Name the blood parasite species.
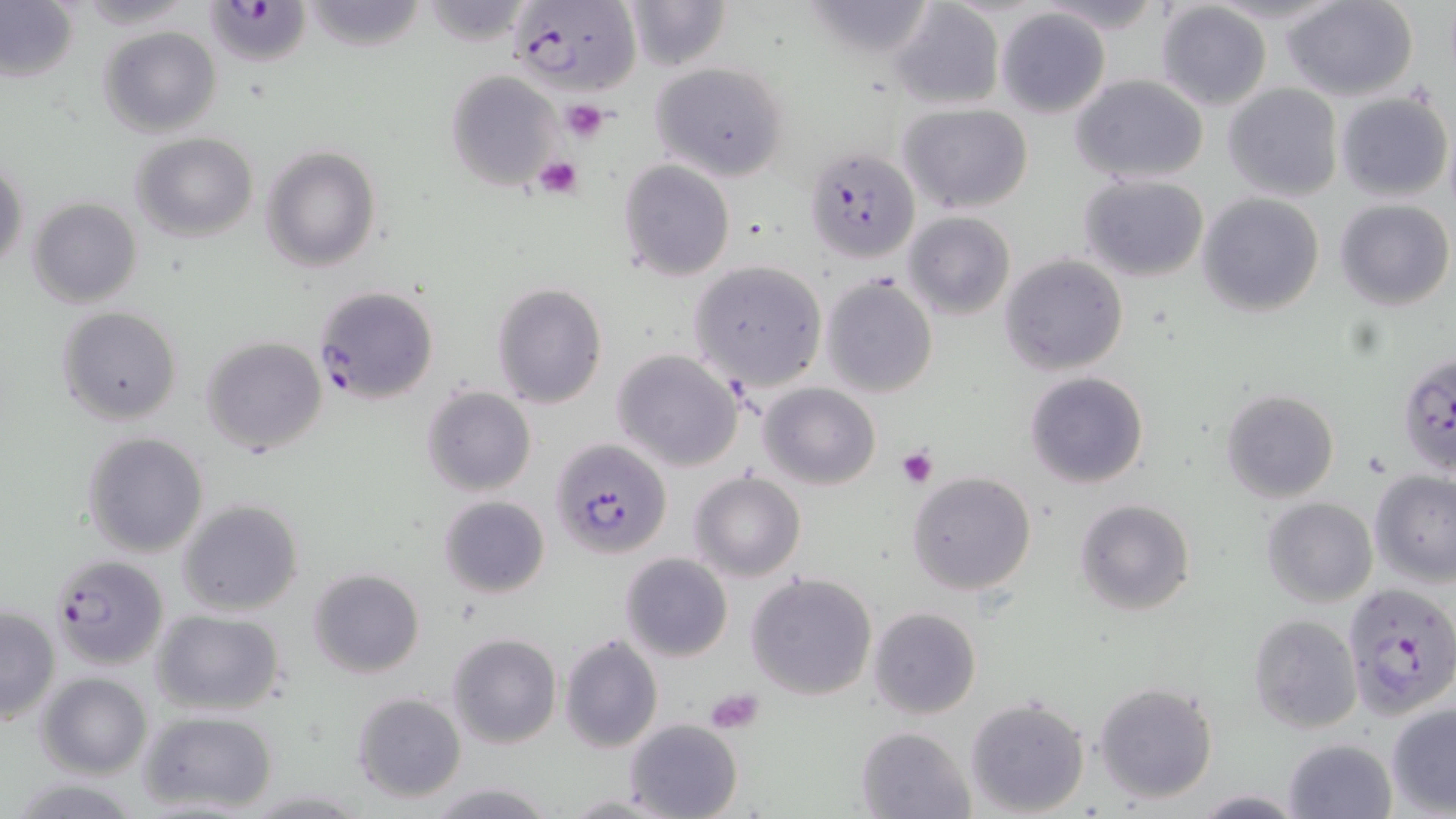

Plasmodium falciparum.

Approximate bounding boxes as (x1, y1, x2, y2) in pixels. Uninfected red blood cell locations: (624, 0, 731, 71), (1284, 0, 1419, 102), (301, 1, 428, 51), (799, 1, 939, 61), (889, 2, 1005, 111), (1155, 2, 1271, 112), (0, 3, 79, 83), (995, 8, 1111, 119), (98, 26, 222, 137), (650, 62, 789, 181), (444, 70, 561, 193), (1070, 75, 1208, 186), (1223, 82, 1344, 201), (1336, 91, 1451, 202), (900, 103, 1033, 214), (130, 132, 258, 241), (262, 145, 380, 273), (1, 156, 28, 276), (617, 158, 736, 281), (1079, 174, 1209, 281), (1197, 192, 1324, 316), (28, 196, 143, 307), (1336, 198, 1453, 310), (904, 211, 1015, 321), (1000, 255, 1128, 374), (687, 260, 828, 392), (822, 275, 939, 397), (492, 281, 606, 407), (58, 306, 182, 426), (202, 336, 327, 456), (612, 348, 744, 472), (1025, 372, 1150, 490), (760, 382, 879, 490), (422, 385, 536, 496), (1221, 388, 1339, 501), (82, 432, 207, 558), (690, 470, 805, 582), (1371, 470, 1456, 585), (907, 471, 1037, 595), (438, 495, 551, 600), (1262, 497, 1378, 606), (177, 498, 304, 616), (1075, 499, 1196, 617), (620, 552, 733, 662), (308, 568, 426, 679), (746, 572, 878, 700), (0, 605, 60, 725), (868, 607, 980, 719), (150, 609, 288, 718), (1249, 615, 1362, 733), (447, 633, 561, 748), (560, 634, 663, 753), (36, 671, 153, 779), (1093, 681, 1218, 804), (352, 691, 467, 803), (964, 694, 1091, 817), (1386, 703, 1456, 815), (136, 709, 280, 815), (625, 719, 744, 819), (856, 725, 976, 818), (1285, 737, 1395, 818), (1, 777, 150, 818), (426, 782, 558, 818), (242, 788, 373, 817), (1191, 791, 1308, 818), (561, 794, 669, 817). Platelet locations: (563, 100, 610, 143), (534, 154, 584, 199), (896, 446, 938, 488), (705, 687, 765, 734). Plasmodium falciparum-infected red blood cell locations: (205, 0, 319, 68), (508, 0, 642, 97), (805, 144, 919, 263), (312, 284, 438, 406), (1397, 354, 1456, 482), (551, 438, 671, 559), (49, 553, 169, 671), (1342, 582, 1456, 717). Thin blood film. Optical microscopy. Captured at 1000x magnification. May-Grünwald-Giemsa-stained preparation. Image is 1456×819 pixels. Single field of view.